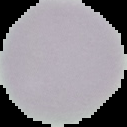

Summary:
  - Image size: 127×127 pixels
  - Preparation: thin blood film
  - Result: no Plasmodium parasites detected
  - Image type: segmented cell region on a black background